Name the blood parasite species.
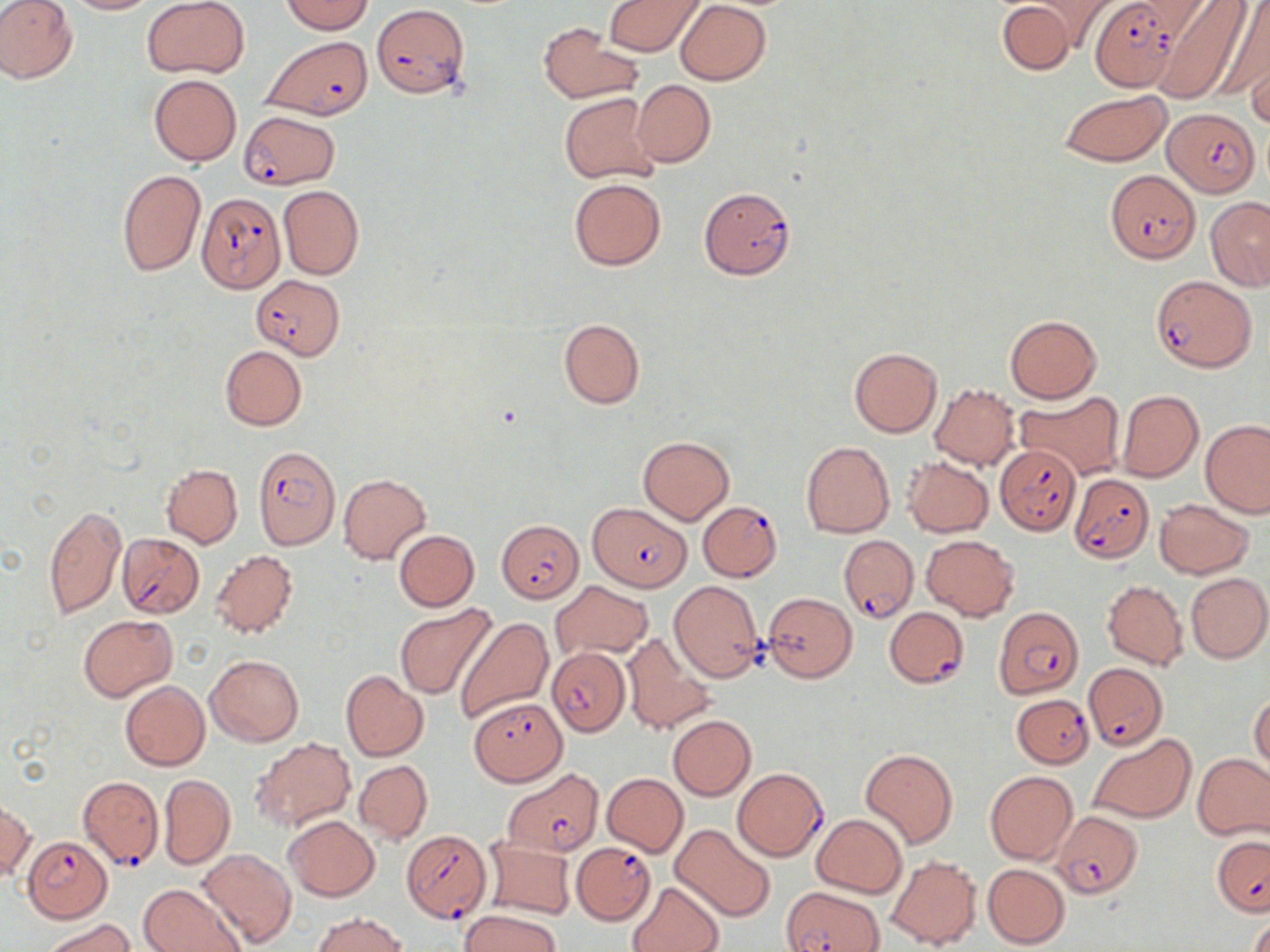

Plasmodium falciparum.

Approximate bounding boxes as (x1,y1)-(x2,y2) corner pairs in pixels. Plasmodium falciparum-infected red blood cell locations: (1091,0)-(1180,90), (371,4)-(470,99), (261,36)-(373,119), (1164,107)-(1259,197), (239,110)-(340,189), (1104,169)-(1200,264), (699,186)-(796,280), (196,193)-(287,294), (253,275)-(346,360), (1151,275)-(1256,372), (998,443)-(1082,534), (252,446)-(340,550), (1068,473)-(1154,562), (698,500)-(783,581), (587,502)-(687,590), (499,520)-(584,603), (117,533)-(204,618), (838,534)-(916,622), (885,607)-(969,687), (993,607)-(1085,699), (545,644)-(629,735), (1082,663)-(1169,749), (1012,693)-(1095,768), (470,697)-(565,784), (733,768)-(827,860), (501,769)-(603,857), (77,776)-(163,869), (1052,810)-(1143,899), (401,831)-(491,922), (1212,834)-(1270,917), (23,836)-(112,922), (572,842)-(655,923), (784,885)-(885,951). Uninfected red blood cell locations: (58,0)-(157,15), (142,0)-(250,79), (274,0)-(377,67), (605,0)-(703,56), (1028,0)-(1121,52), (1127,0)-(1214,46), (0,1)-(78,84), (281,1)-(374,34), (996,1)-(1078,75), (1151,1)-(1250,104), (675,2)-(769,85), (1214,3)-(1270,106), (537,23)-(644,104), (1246,54)-(1270,130), (148,74)-(241,166), (631,79)-(715,167), (1058,89)-(1171,166), (558,91)-(659,185), (117,169)-(206,276), (569,177)-(665,270), (278,185)-(364,280), (1206,197)-(1270,290), (1005,315)-(1101,404), (558,318)-(644,408), (220,345)-(307,430), (849,347)-(942,437), (929,383)-(1020,470), (1015,390)-(1125,480), (1116,390)-(1204,482), (1201,419)-(1269,518), (638,436)-(733,524), (801,441)-(895,538), (902,457)-(994,537), (161,463)-(242,547), (338,473)-(431,565), (1153,498)-(1254,579), (41,505)-(126,618), (393,529)-(480,611), (922,534)-(1019,619), (210,549)-(298,640), (1185,572)-(1269,662), (669,580)-(766,682), (1103,580)-(1188,669), (551,581)-(653,660), (764,592)-(857,681), (394,605)-(496,699), (78,615)-(176,701), (452,615)-(555,725), (621,632)-(715,736), (205,654)-(303,746), (341,671)-(428,761), (120,680)-(209,771), (1249,694)-(1270,774), (667,715)-(755,800), (1088,734)-(1196,824), (250,737)-(355,833), (861,748)-(957,848), (1193,753)-(1270,841), (354,759)-(432,845), (984,771)-(1078,865), (164,773)-(248,946), (602,773)-(688,856), (160,774)-(235,868), (0,800)-(32,881), (813,814)-(907,897), (284,815)-(379,900), (671,823)-(776,921), (483,837)-(576,919), (197,848)-(297,948), (885,853)-(981,949), (982,863)-(1070,948), (140,880)-(243,952), (628,881)-(725,952), (461,910)-(560,952), (312,912)-(406,952), (1248,914)-(1270,952), (42,918)-(138,952). Image is 1270×952 pixels. 1000x magnification. Single field of view. Light microscopy. May-Grünwald-Giemsa stain. Thin blood film.